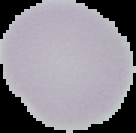
image type = segmented cell region with the area outside set to black
preparation = thin blood smear
result = no Plasmodium parasites seen
image size = 136×133 pixels